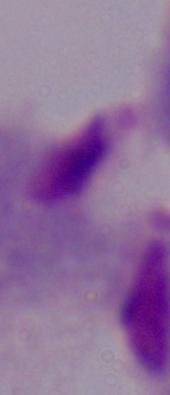

modality = micrograph
identification = trichomonad
magnification = 1000x